Assess this cell for malaria.
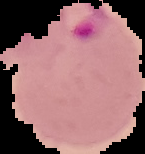
Parasitized.

From a thin blood film. Cell region segmented out of the field of view; the surrounding area is masked to black. Image is 145×154 pixels.